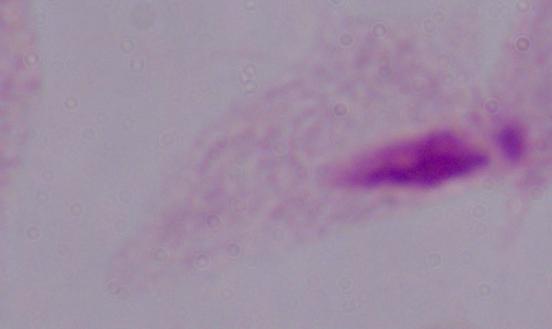
{
  "modality": "micrograph",
  "identification": "trichomonad",
  "magnification": "1000x"
}